Report the malaria status of this cell.
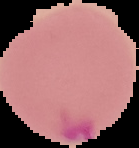
It is parasitized.

preparation = thin blood film
image size = 139×148 pixels
image type = segmented cell region with the area outside set to black